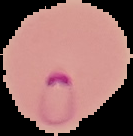 Segmented cell region on a black background. Image is 133×136 pixels. From a thin blood film. Malaria status: parasitized.